Comment on the morphology of the red blood cells.
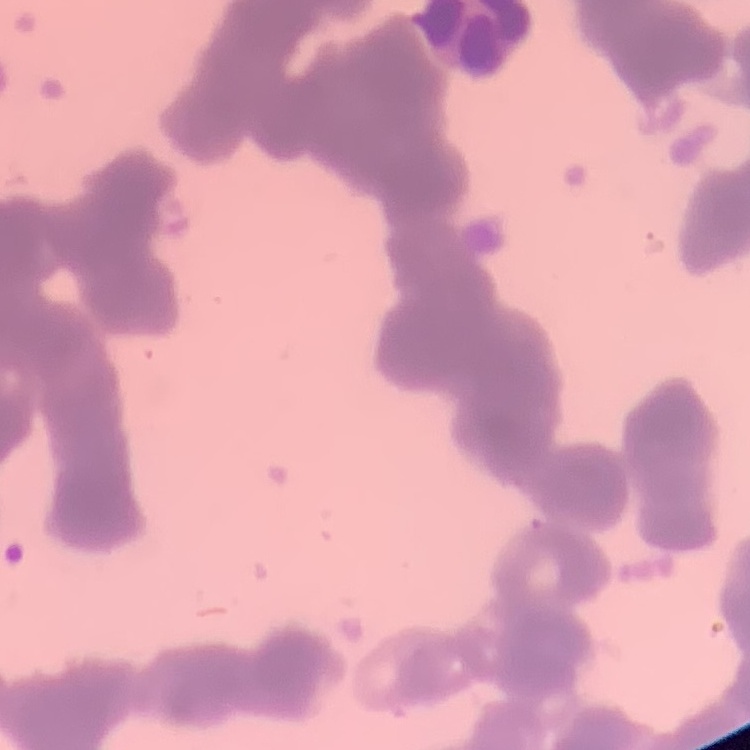
Rouleaux formation.

Square crop of a larger photomicrograph. Thin blood film. Field's or Giemsa stain.